Locate every Plasmodium falciparum parasite and give its life-cycle stage, and locate every leukocyte and any debris.
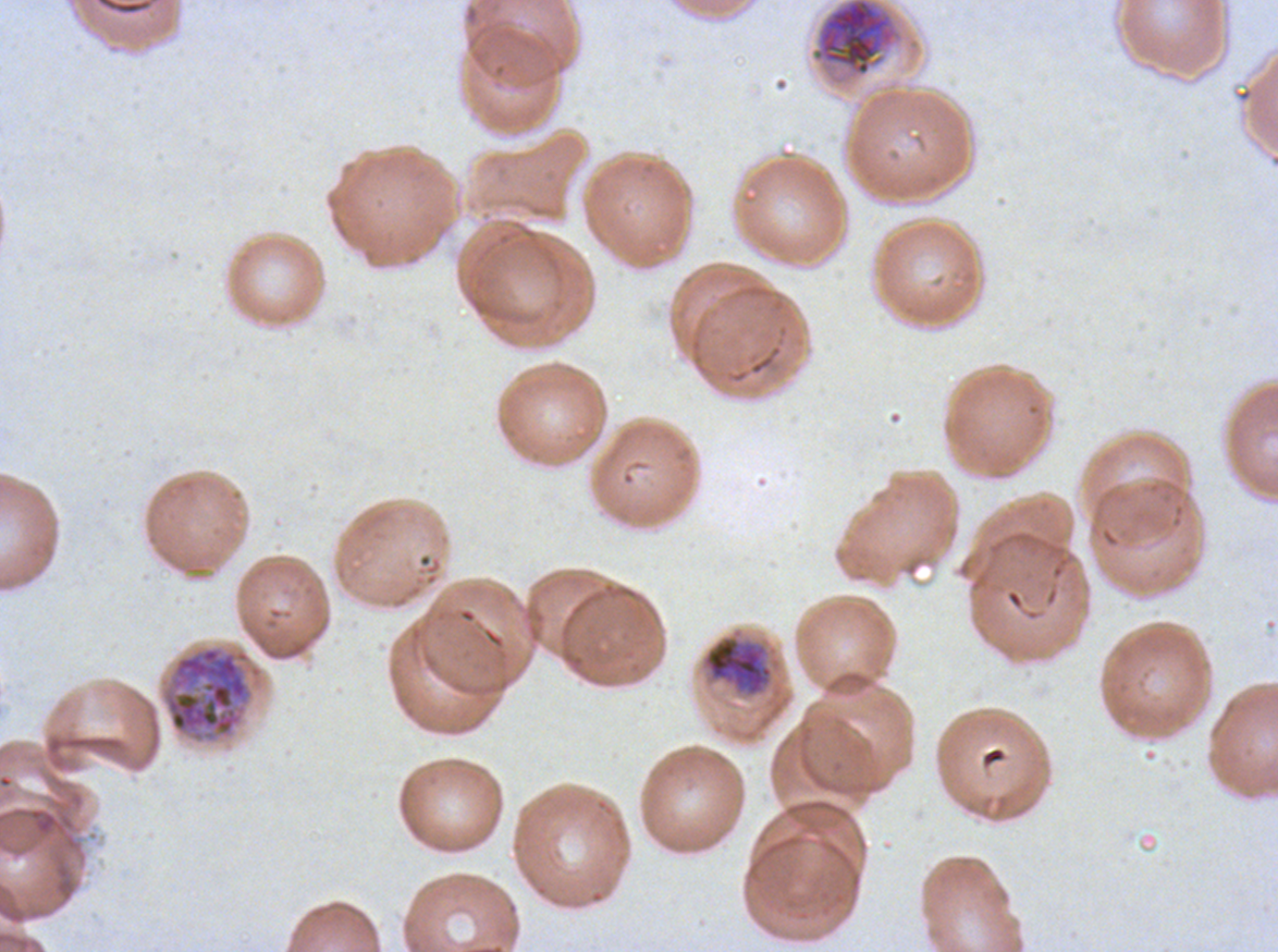
Approximate bounding boxes as {x1, y1, x2, y2} in pixels.
Early schizonts: {694, 624, 796, 740}, {163, 645, 252, 741}.
Late schizonts: {813, 0, 899, 77}.
No rings, late-ring/early-trophozoite forms, mid trophozoites, late trophozoites, segmenters, gametocytes, leukocytes, or debris observed.

{
  "specimen": "ex-vivo Plasmodium falciparum culture from a patient in The Gambia, grown for 24 to 48 hours",
  "preparation": "thin blood film",
  "life_cycle_stages_observed": "early schizont, late schizont",
  "field_of_view": "one sub-image of a larger composite",
  "image_size": "1278×952 pixels",
  "stain": "Giemsa"
}